Assess the morphology of the red blood cells.
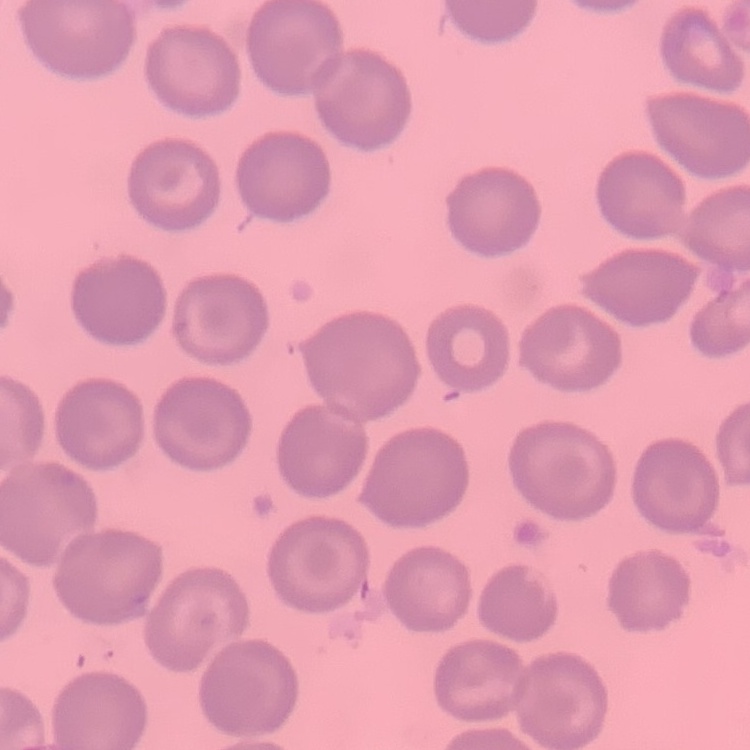

No rouleaux formation.

preparation = thin blood film
image type = square crop of a larger photomicrograph
stain = Field's or Giemsa